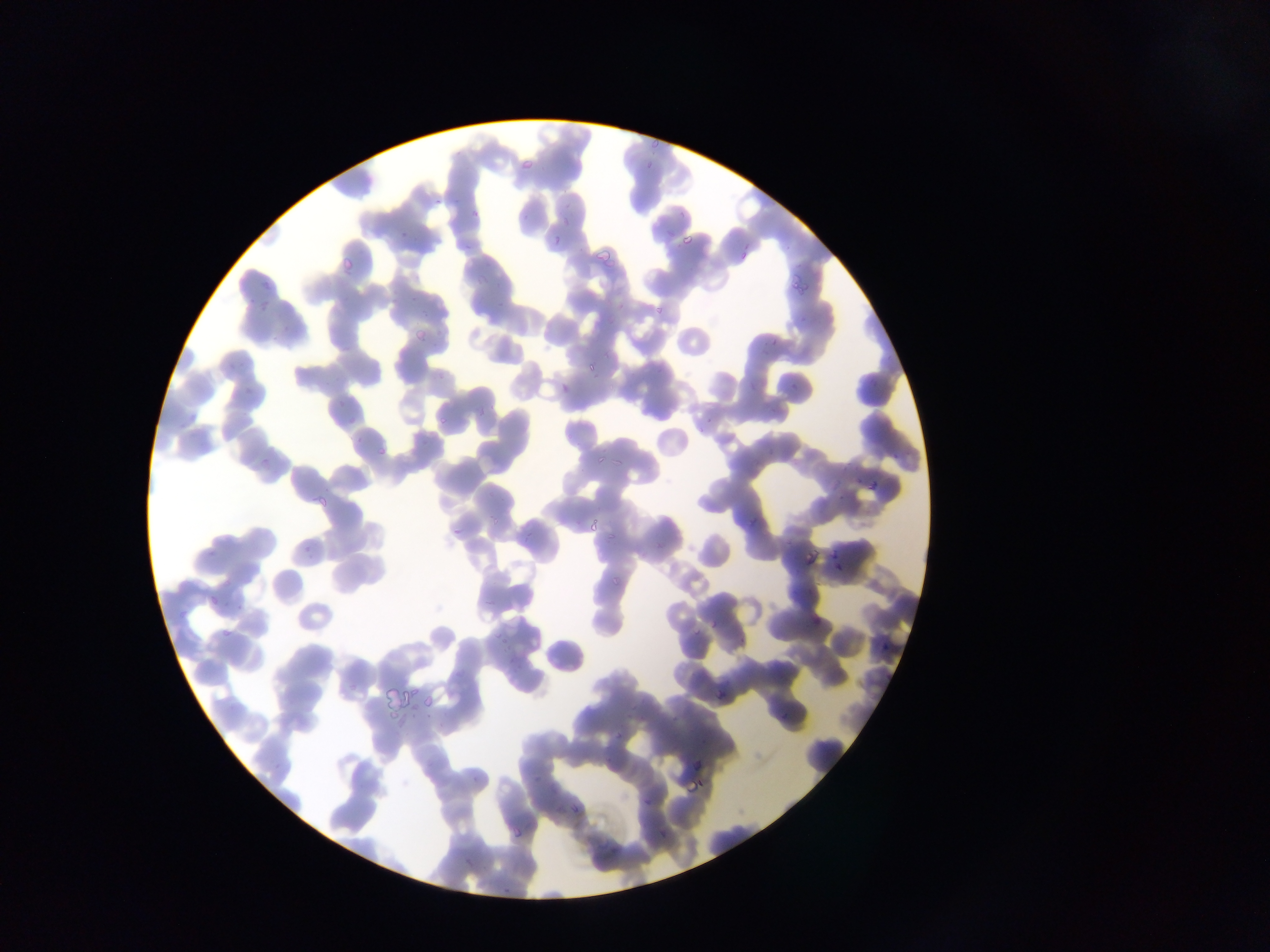

Approximate bounding boxes as {left, top, right, bottom} in pixels.
Summary:
  - Malaria parasite locations: {647, 138, 661, 147}, {519, 158, 533, 168}, {644, 161, 654, 170}, {432, 198, 443, 206}, {563, 214, 570, 224}, {398, 228, 406, 239}, {554, 232, 560, 242}, {681, 232, 695, 248}, {590, 244, 617, 260}, {340, 251, 358, 267}, {790, 273, 814, 293}, {258, 297, 270, 310}, {653, 306, 668, 312}, {414, 327, 428, 345}, {587, 364, 595, 371}, {559, 380, 571, 395}, {480, 403, 484, 417}, {439, 414, 447, 424}, {377, 443, 387, 457}, {596, 457, 604, 463}, {612, 460, 622, 467}, {866, 478, 878, 490}, {314, 494, 328, 513}, {590, 521, 601, 530}, {453, 526, 461, 538}, {608, 531, 617, 541}, {803, 544, 817, 566}, {826, 550, 838, 560}, {612, 576, 623, 586}, {210, 597, 218, 611}, {708, 619, 719, 629}, {220, 625, 232, 638}, {686, 628, 707, 637}, {408, 687, 418, 696}, {711, 687, 726, 700}, {421, 690, 438, 711}, {612, 731, 624, 740}, {696, 774, 705, 788}, {684, 781, 698, 794}, {641, 796, 655, 805}, {571, 803, 585, 813}, {557, 806, 565, 816}, {514, 820, 525, 840}, {657, 827, 667, 841}, {501, 887, 514, 896} | approximate {x, y} pixel centers of objects too small to bound: {475, 214}
  - Country: Ghana
  - Preparation: thin blood smear
  - Image size: 1270×952 pixels
  - Field of view: single
  - Capture: mobile-phone photograph through a microscope